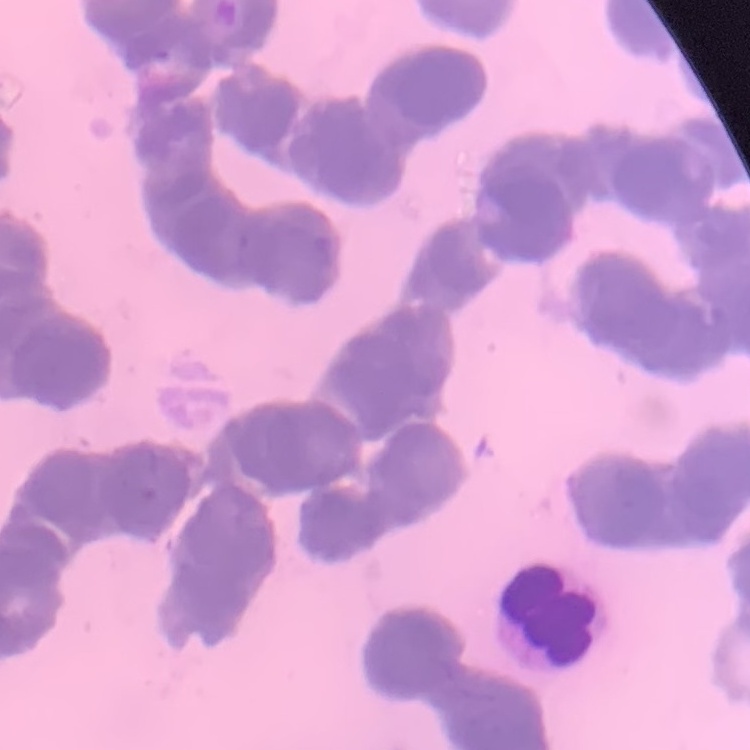

red blood cell morphology = rouleaux formation
stain = Field's or Giemsa
image type = one tile cut from a larger photomicrograph
preparation = thin blood film